Name the cell type shown.
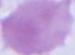
This is an erythrocyte.

Summary:
  - Modality: photomicrograph
  - Magnification: 1000x